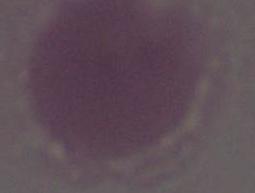

1000x magnification. Micrograph. An erythrocyte is shown.